Locate the cells, classifying each as a parasitized red blood cell, an uninfected red blood cell, or a white blood cell.
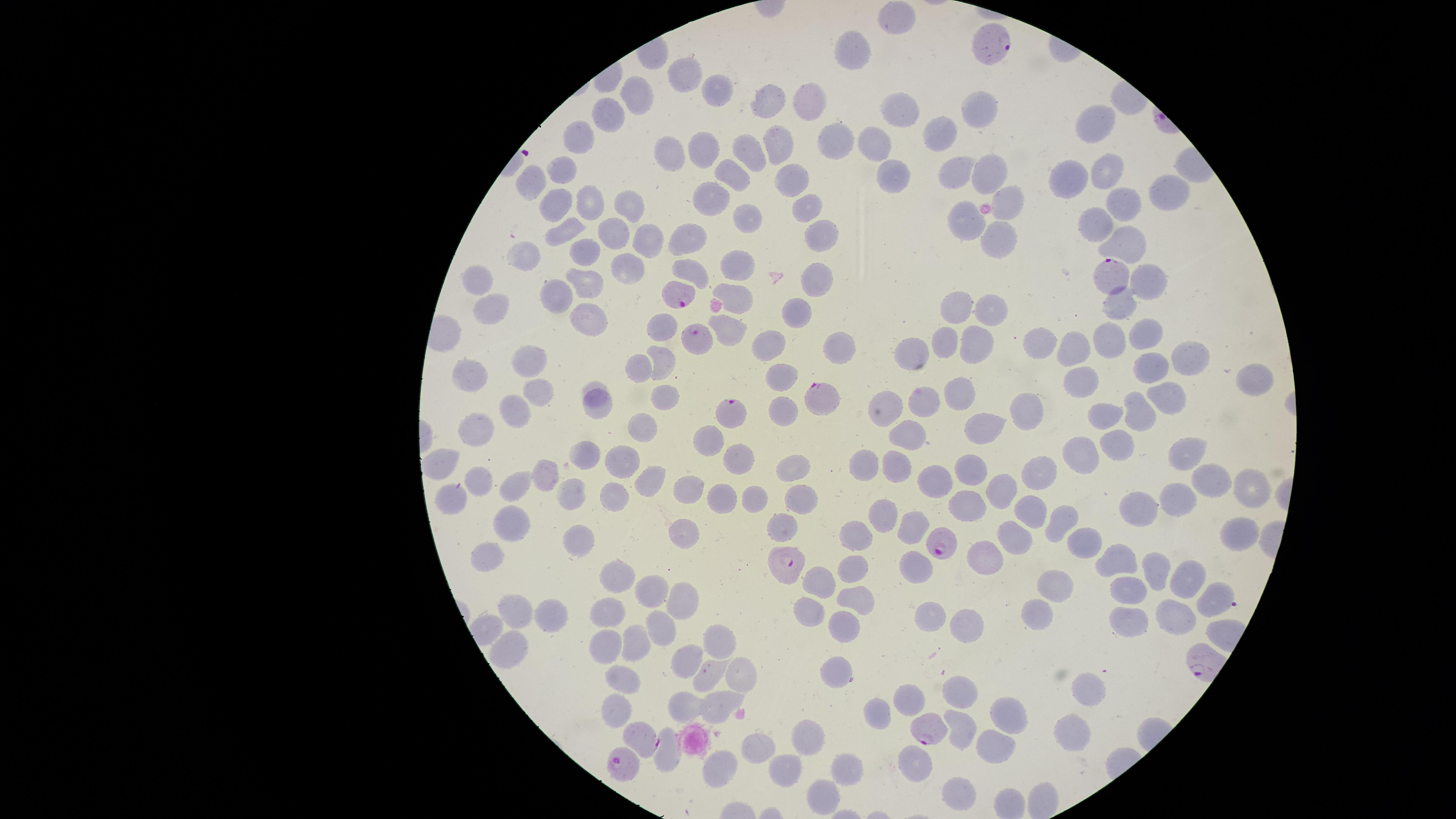

Approximate marker points, in pixels from the top-left corner.
Parasitized red blood cells: (x=990, y=43), (x=1109, y=276), (x=678, y=294), (x=698, y=338), (x=822, y=397), (x=729, y=412), (x=941, y=546), (x=789, y=569), (x=926, y=729), (x=636, y=736), (x=624, y=767).
Uninfected red blood cells: (x=895, y=19), (x=857, y=50), (x=692, y=74), (x=718, y=89), (x=638, y=96), (x=771, y=102), (x=811, y=103), (x=980, y=107), (x=902, y=109), (x=612, y=112), (x=1100, y=123), (x=835, y=133), (x=943, y=133), (x=583, y=141), (x=779, y=141), (x=878, y=145), (x=697, y=148), (x=666, y=151), (x=750, y=151), (x=565, y=167), (x=891, y=169), (x=1109, y=171), (x=990, y=172), (x=958, y=173), (x=736, y=176), (x=532, y=177), (x=1071, y=177), (x=792, y=180), (x=1011, y=195), (x=1168, y=195), (x=584, y=198), (x=717, y=201), (x=624, y=202), (x=551, y=203), (x=806, y=206), (x=1126, y=206), (x=745, y=218), (x=972, y=219), (x=1102, y=221), (x=570, y=224), (x=612, y=229), (x=824, y=233), (x=1003, y=236), (x=653, y=237), (x=690, y=237), (x=1128, y=239), (x=586, y=254), (x=536, y=255), (x=738, y=267), (x=628, y=269), (x=698, y=273), (x=586, y=277), (x=480, y=279), (x=1150, y=280), (x=821, y=281), (x=560, y=291), (x=741, y=294), (x=1123, y=304), (x=961, y=307), (x=991, y=307), (x=490, y=311), (x=796, y=311), (x=593, y=321), (x=662, y=328), (x=734, y=330), (x=1147, y=332), (x=1117, y=340), (x=977, y=342), (x=943, y=343), (x=1044, y=343), (x=772, y=346), (x=842, y=346), (x=1073, y=346), (x=914, y=347), (x=1189, y=356), (x=665, y=359), (x=529, y=364), (x=639, y=369), (x=1148, y=370), (x=780, y=371), (x=470, y=374), (x=1086, y=380), (x=1253, y=381), (x=595, y=384), (x=958, y=389), (x=539, y=392), (x=670, y=397), (x=1176, y=397), (x=926, y=402), (x=887, y=405), (x=516, y=408), (x=600, y=408), (x=785, y=408), (x=1031, y=409), (x=1140, y=410), (x=1110, y=414), (x=987, y=425), (x=643, y=427), (x=476, y=430), (x=909, y=434), (x=713, y=437), (x=1116, y=447), (x=1190, y=451), (x=738, y=457), (x=1081, y=457), (x=442, y=462), (x=585, y=462), (x=624, y=462), (x=866, y=464), (x=797, y=467), (x=968, y=469), (x=892, y=470), (x=1041, y=471), (x=540, y=474), (x=655, y=476), (x=943, y=479), (x=1207, y=479), (x=482, y=482), (x=992, y=487), (x=519, y=488), (x=1249, y=488), (x=687, y=489), (x=751, y=491), (x=722, y=494), (x=611, y=496), (x=454, y=497), (x=805, y=497), (x=1179, y=498), (x=572, y=499), (x=968, y=502), (x=1031, y=502), (x=1142, y=511), (x=880, y=513), (x=1058, y=518), (x=509, y=524), (x=783, y=527), (x=1237, y=527), (x=910, y=529), (x=684, y=530), (x=857, y=533), (x=1018, y=535), (x=1078, y=541), (x=577, y=542), (x=495, y=553), (x=986, y=555), (x=1118, y=559), (x=914, y=562), (x=854, y=564), (x=1157, y=571), (x=815, y=576), (x=1183, y=577), (x=623, y=583), (x=1058, y=588), (x=655, y=589), (x=1130, y=593), (x=683, y=598), (x=853, y=598), (x=1211, y=602), (x=515, y=607), (x=614, y=607), (x=810, y=607), (x=1041, y=608), (x=931, y=612), (x=1127, y=613), (x=1175, y=613), (x=554, y=615), (x=968, y=615), (x=660, y=623), (x=841, y=626), (x=604, y=638), (x=718, y=638), (x=635, y=642), (x=506, y=647), (x=681, y=659), (x=627, y=670), (x=838, y=671), (x=738, y=675), (x=707, y=678), (x=1086, y=688), (x=958, y=692), (x=910, y=701), (x=616, y=704), (x=873, y=707), (x=1012, y=707), (x=681, y=712), (x=720, y=713), (x=1071, y=727), (x=959, y=729), (x=807, y=735), (x=759, y=747), (x=996, y=749), (x=664, y=757), (x=918, y=757), (x=716, y=761), (x=844, y=768), (x=790, y=771), (x=959, y=787), (x=823, y=797).
No white blood cells identified.

Circular visible region. Species: Plasmodium falciparum. Image is 1456×819 pixels. Thin smear of blood. Single field of view. Giemsa stain. Photographed with a smartphone camera through the microscope eyepiece.